Report the malaria status of this cell.
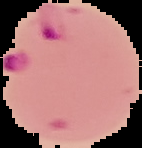
Parasitized.

Summary:
  - Image type: cell region segmented out of the field of view; surrounding area masked to black
  - Image size: 142×148 pixels
  - Preparation: thin blood smear